Report the malaria status of this cell.
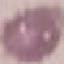

Uninfected.

Photographed with a smartphone camera at the microscope eyepiece. Automatically extracted cell patch, resized to 64 × 64 pixels. Giemsa stain. Thin blood smear.